Locate every blood parasite and identify its species.
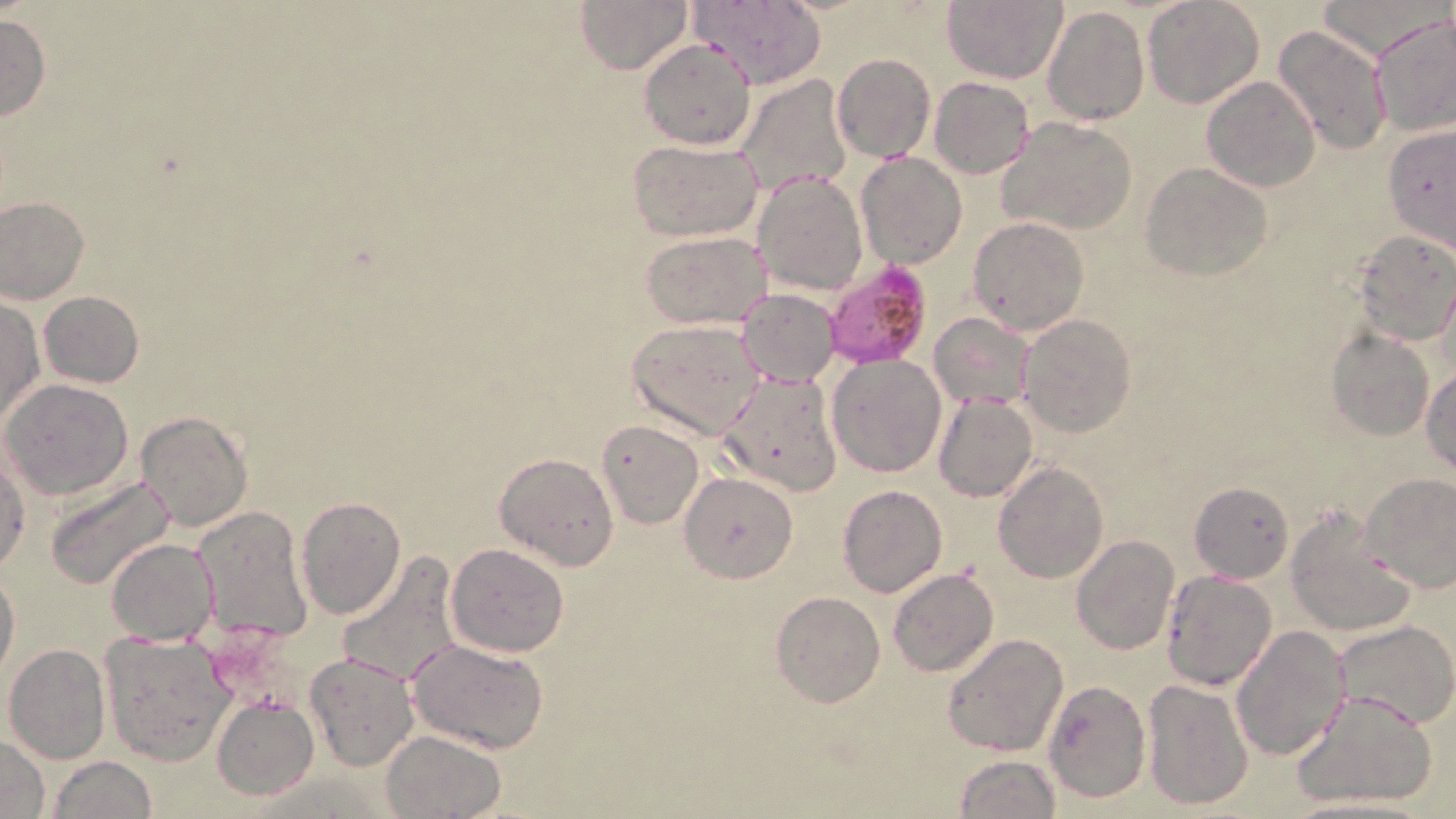
Approximate bounding boxes as (x1, y1, x2, y2) in pixels.
Plasmodium falciparum-infected red blood cells (subset): (824, 259, 932, 368).
No Plasmodium ovale, Plasmodium malariae, Plasmodium vivax, Babesia divergens, or Trypanosoma brucei observed.

slide-level diagnosis = Plasmodium falciparum
field of view = one of a larger specimen
magnification = 1000x
image size = 1456×819 pixels
uninfected red blood cell locations (subset) = approximate bounding boxes as (x1, y1, x2, y2) in pixels: (576, 0, 691, 74), (686, 0, 826, 89), (1142, 0, 1265, 110), (1317, 0, 1442, 62), (942, 1, 1066, 83), (1042, 5, 1148, 125), (0, 15, 51, 121), (1372, 16, 1455, 137), (1271, 23, 1393, 158), (639, 38, 757, 151), (832, 52, 935, 163), (734, 74, 852, 198), (1201, 75, 1321, 191), (929, 77, 1034, 178), (998, 117, 1139, 236), (1383, 126, 1456, 254), (627, 139, 763, 240), (855, 152, 967, 268), (1141, 162, 1273, 280), (752, 172, 867, 294), (0, 196, 90, 304), (967, 217, 1089, 335), (1352, 229, 1455, 346), (642, 230, 771, 327), (735, 288, 839, 388), (39, 291, 144, 386), (0, 298, 44, 423), (928, 311, 1037, 409), (1019, 314, 1136, 437), (627, 318, 765, 439), (1325, 328, 1434, 441), (827, 354, 946, 477), (1421, 367, 1455, 473), (721, 371, 844, 495), (1, 379, 134, 499), (933, 392, 1038, 503), (137, 411, 252, 531), (597, 420, 704, 530), (0, 447, 30, 574), (495, 452, 619, 570), (992, 463, 1109, 584), (679, 472, 798, 582), (1361, 472, 1456, 592), (44, 473, 176, 591), (1189, 481, 1294, 584), (837, 484, 949, 597), (296, 496, 406, 621), (192, 505, 315, 645), (1286, 508, 1415, 638), (1071, 536, 1180, 656), (106, 538, 219, 645), (444, 543, 570, 658), (335, 550, 463, 688), (1, 568, 20, 682), (887, 569, 998, 677), (1162, 570, 1277, 690), (772, 592, 886, 708), (1333, 620, 1455, 730), (1231, 624, 1350, 760), (100, 630, 238, 766), (942, 632, 1069, 757), (407, 637, 552, 754), (3, 644, 110, 764), (302, 651, 419, 772), (1141, 677, 1253, 811), (1291, 689, 1441, 811), (213, 696, 319, 800), (381, 730, 508, 819), (0, 735, 51, 818), (953, 755, 1061, 818), (48, 756, 159, 818), (1279, 796, 1439, 818)
preparation = thin blood film
modality = optical microscopy
stain = May-Grünwald-Giemsa